Locate every Plasmodium parasite.
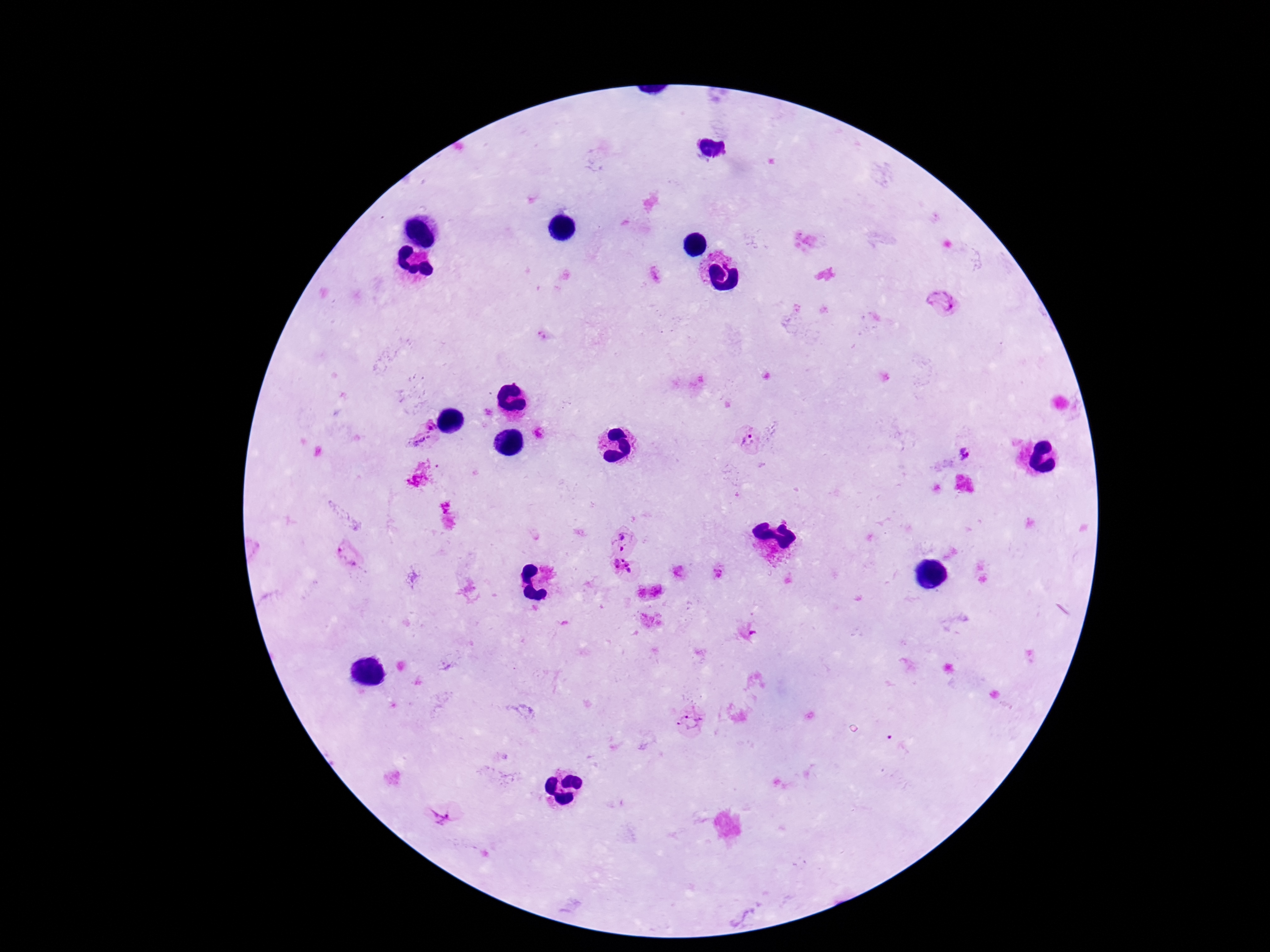
Approximate centers as {x, y} in pixels.
Plasmodium parasites: {941, 303}, {431, 426}, {748, 441}, {421, 443}, {965, 455}, {622, 539}, {347, 553}, {621, 568}, {692, 721}, {444, 816}.

Image is 1270×952 pixels. Photographed through the microscope eyepiece with a smartphone camera. Giemsa stain. Patient malaria status: infected. One field from this slide. 100x magnification. Thick blood film.